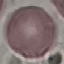

Summary:
  - Malaria status: uninfected
  - Preparation: thin blood film
  - Capture: smartphone camera at the microscope eyepiece
  - Stain: Giemsa
  - Image type: automatically extracted cell patch, resized to 64 × 64 pixels